Point out each Plasmodium parasite.
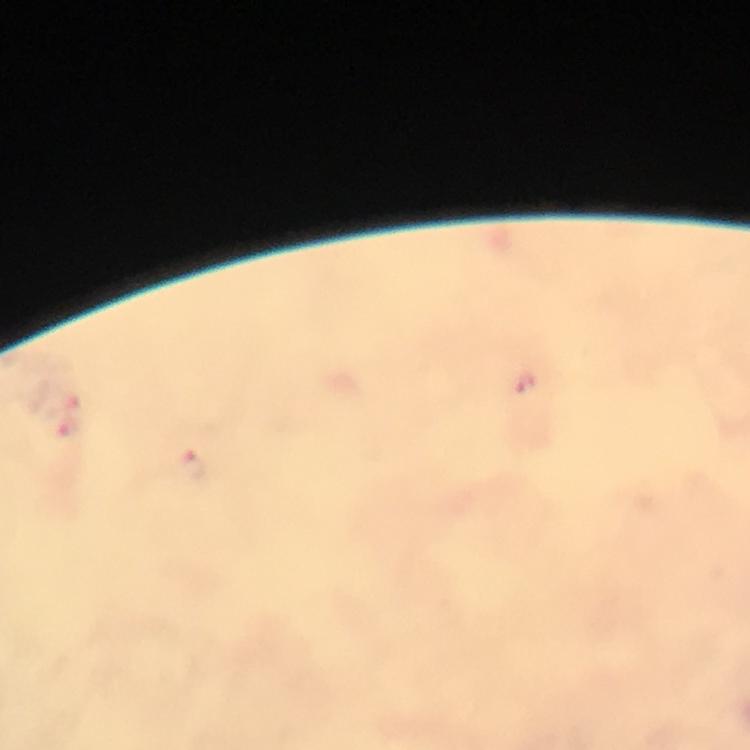
Approximate centers as [x, y] in pixels.
Plasmodium parasites: [523, 380], [194, 465].

context = from a malaria diagnostic workup
stain = Giemsa
magnification = 100x
capture = smartphone mounted on the microscope
cropped from = a single field of view
image size = 750×750 pixels
immersion oil = applied
preparation = thick blood smear